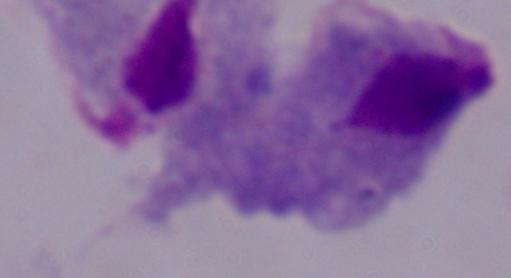
Summary:
  - Magnification: 1000x
  - Modality: micrograph
  - Identification: trichomonad